Point out each Plasmodium parasite and each leukocyte.
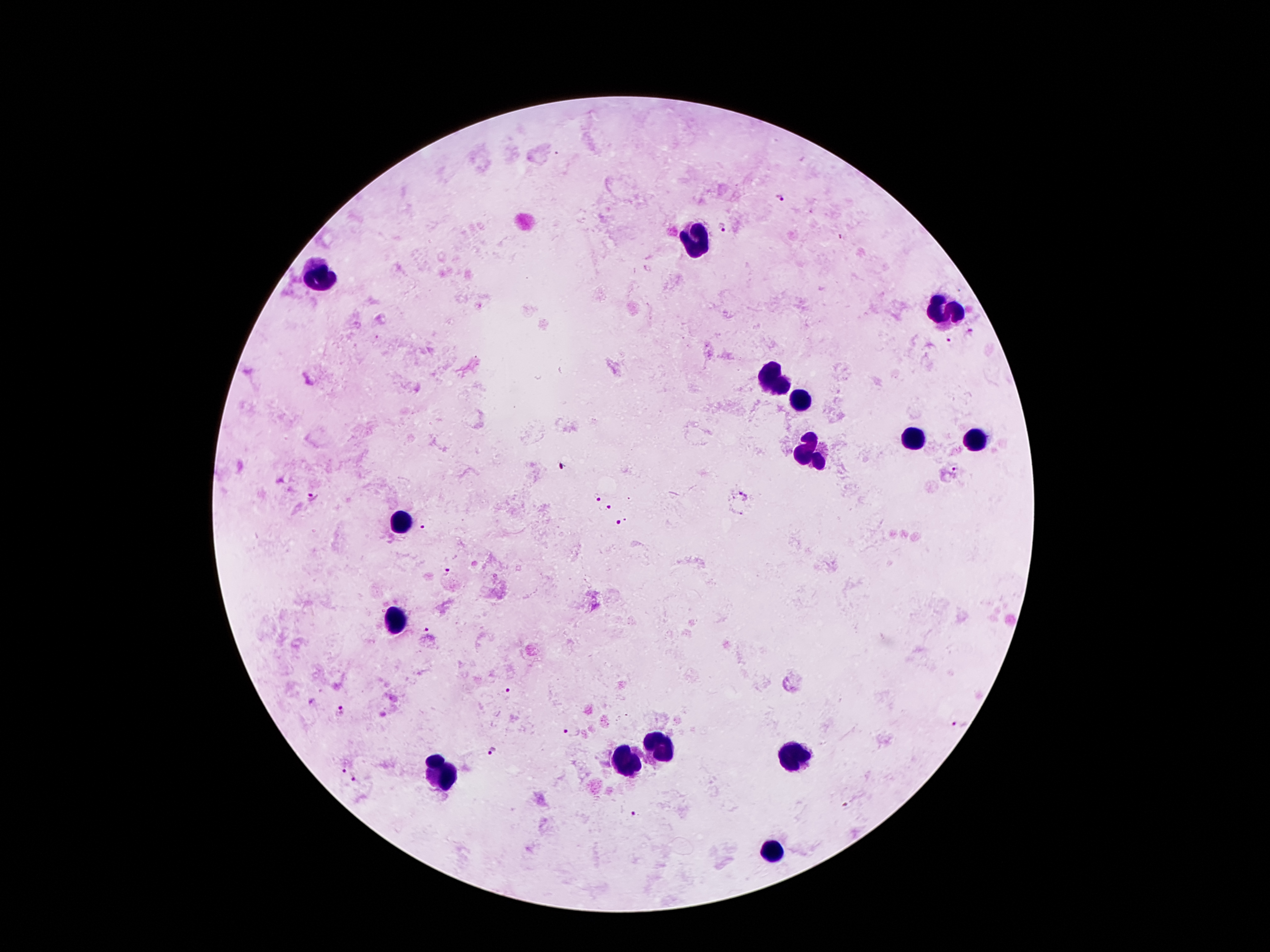
Approximate centers as {x, y} in pixels.
Plasmodium parasites: {780, 199}, {721, 229}, {843, 238}, {970, 332}, {946, 336}, {560, 467}, {955, 470}, {314, 495}, {741, 496}, {596, 497}, {606, 507}, {622, 520}, {423, 529}, {447, 572}, {423, 629}, {507, 691}, {311, 702}, {341, 709}, {958, 725}, {568, 732}, {494, 752}, {342, 769}, {357, 780}, {848, 806}, {634, 815}.
Leukocytes: {695, 237}, {321, 275}, {947, 308}, {775, 377}, {802, 399}, {909, 436}, {976, 440}, {808, 455}, {403, 520}, {397, 623}, {659, 749}, {796, 756}, {626, 758}, {445, 772}, {773, 852}.

Summary:
  - Capture: smartphone camera through the microscope eyepiece
  - Preparation: thick blood smear
  - Patient malaria status: infected with Plasmodium falciparum
  - Image size: 1270×952 pixels
  - Field of view: one from this slide
  - Magnification: 100x
  - Stain: Giemsa